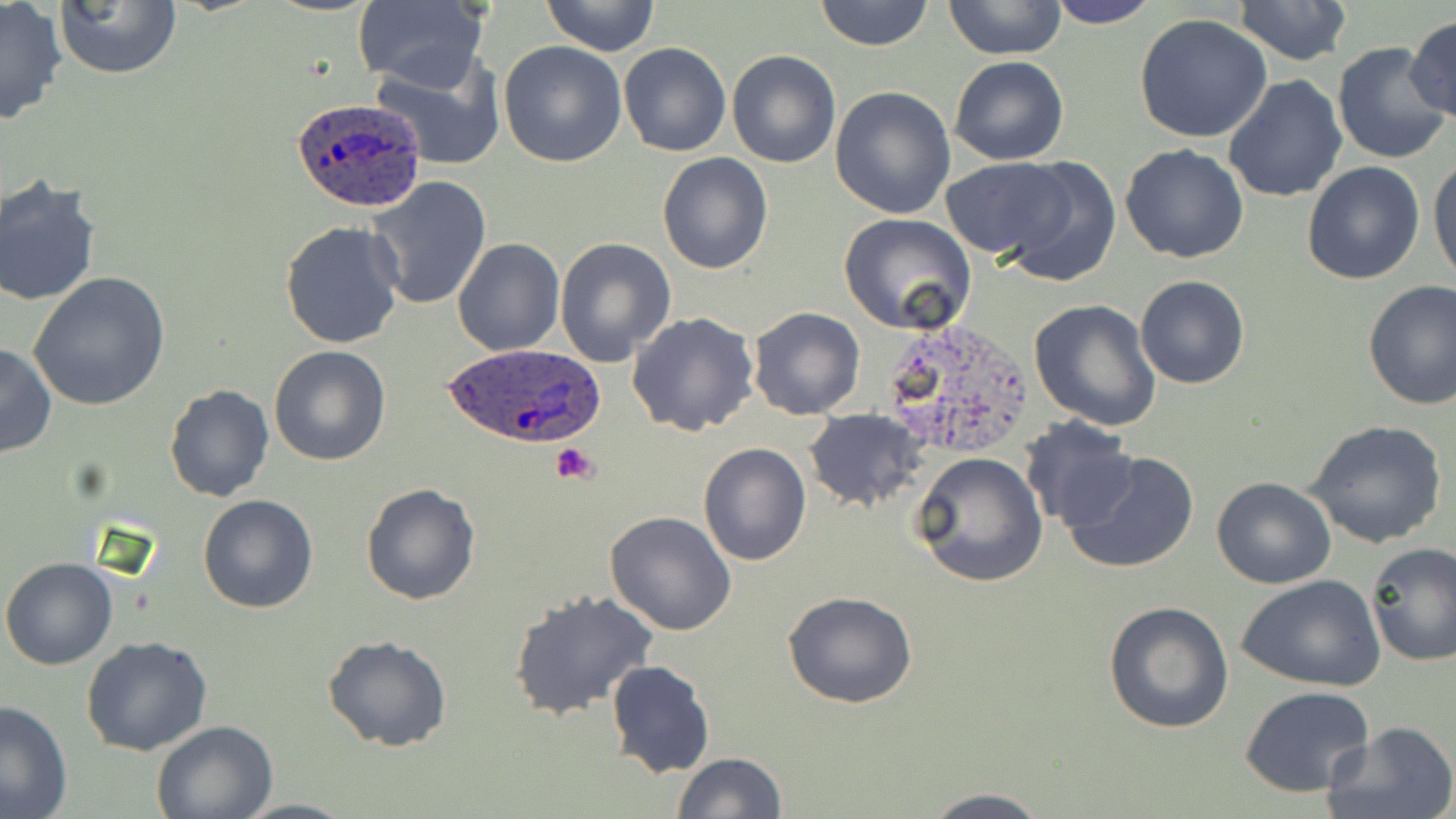
slide-level diagnosis = Plasmodium ovale
image size = 1456×819 pixels
modality = optical microscopy
preparation = thin blood smear
Plasmodium ovale-infected red blood cell locations = approximate bounding boxes as (x1,y1)-(x2,y2) corner pairs in pixels: (290,96)-(426,212), (442,343)-(605,450)
uninfected red blood cell locations = approximate bounding boxes as (x1,y1)-(x2,y2) corner pairs in pixels: (53,0)-(182,80), (540,0)-(660,55), (814,0)-(933,50), (942,0)-(1067,58), (1043,0)-(1160,28), (1233,0)-(1354,66), (0,1)-(69,126), (352,2)-(489,90), (1132,12)-(1274,142), (1405,16)-(1454,124), (498,40)-(627,169), (618,41)-(731,158), (1332,42)-(1453,167), (727,49)-(842,168), (368,51)-(506,170), (949,55)-(1069,166), (1222,76)-(1347,205), (829,86)-(956,219), (1120,143)-(1251,263), (1429,151)-(1456,283), (657,153)-(773,275), (941,157)-(1071,260), (997,157)-(1120,288), (1301,160)-(1427,284), (365,175)-(492,310), (0,177)-(101,306), (839,213)-(977,335), (280,221)-(405,351), (451,237)-(564,356), (553,237)-(677,368), (28,273)-(172,412), (1134,274)-(1250,390), (1361,281)-(1456,410), (1035,284)-(1253,408), (1028,300)-(1161,432), (748,306)-(865,420), (625,310)-(760,436), (0,342)-(55,458), (268,345)-(392,466), (163,383)-(274,503), (802,408)-(927,514), (1020,417)-(1139,530), (1303,419)-(1450,550), (698,443)-(812,567), (1061,450)-(1199,575), (910,451)-(1049,587), (1210,476)-(1338,589), (361,482)-(482,604), (197,493)-(318,615), (604,510)-(737,635), (1365,542)-(1456,667), (0,557)-(119,671), (1237,573)-(1387,693), (508,591)-(661,721), (784,591)-(917,709), (1102,600)-(1235,735), (323,634)-(452,751), (81,635)-(212,756), (606,659)-(715,779), (1240,685)-(1378,798), (0,700)-(72,818), (150,719)-(278,817), (1322,721)-(1456,819), (671,753)-(787,818), (920,789)-(1052,819)
magnification = 1000x
field of view = single
stain = May-Grünwald-Giemsa
platelet locations = approximate bounding boxes as (x1,y1)-(x2,y2) corner pairs in pixels: (550,443)-(599,486)